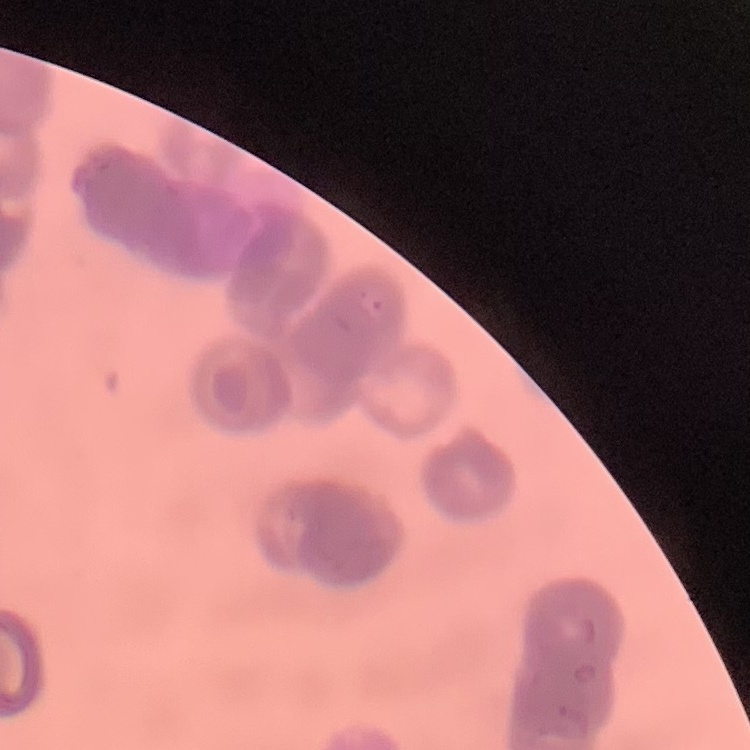

red_blood_cell_morphology: rouleaux formation
image_type: square crop of a larger photomicrograph
stain: Field's or Giemsa
preparation: thin blood film